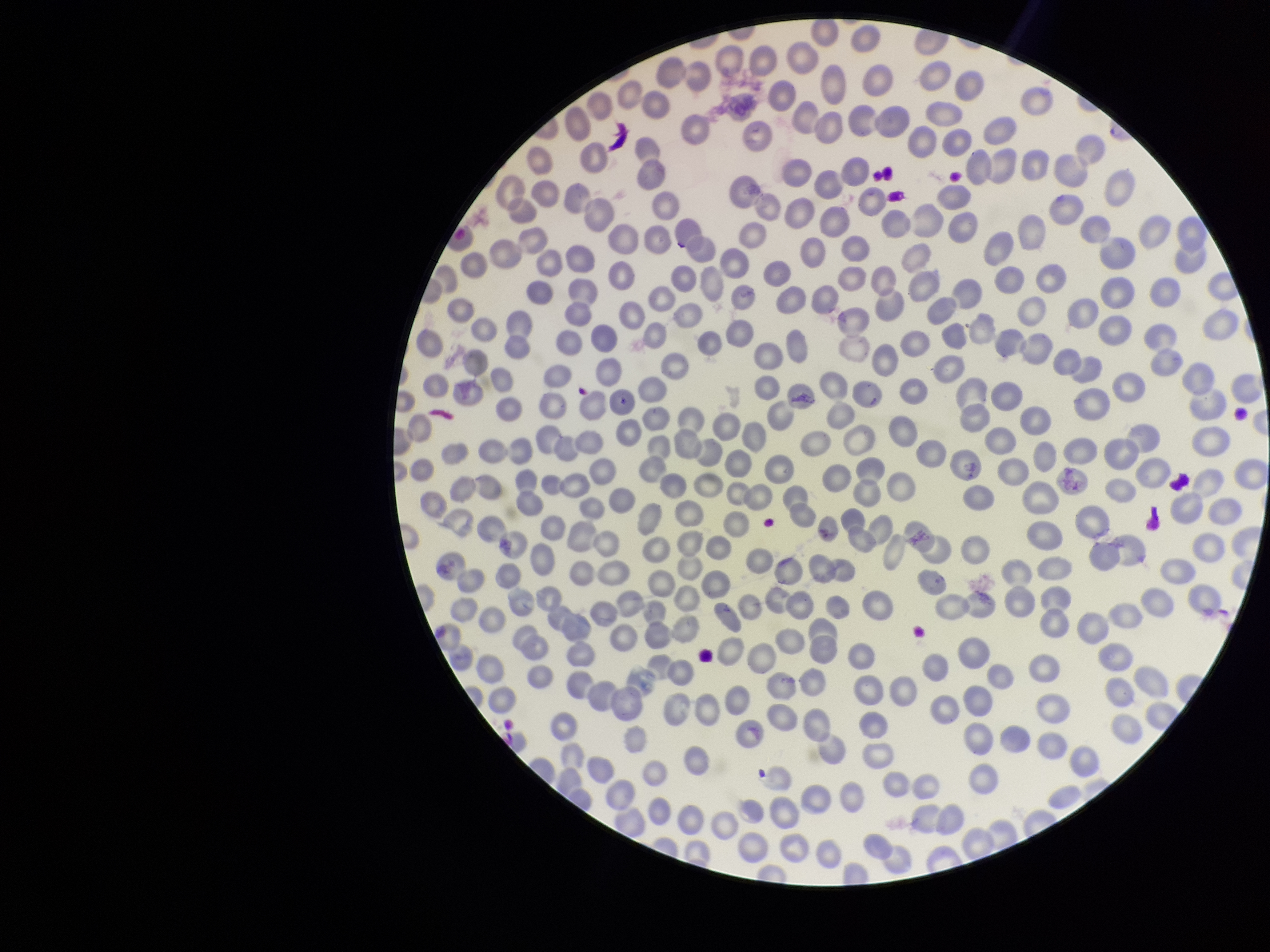

preparation = thin blood smear
stain = Giemsa
parasitized red blood cell count = 0
field of view = one from this slide
red blood cell count = 344
parasitized red blood cells = none detected
patient malaria status = infected
capture = smartphone photograph through the microscope eyepiece
image size = 1270×952 pixels
species reported for this patient = Plasmodium falciparum